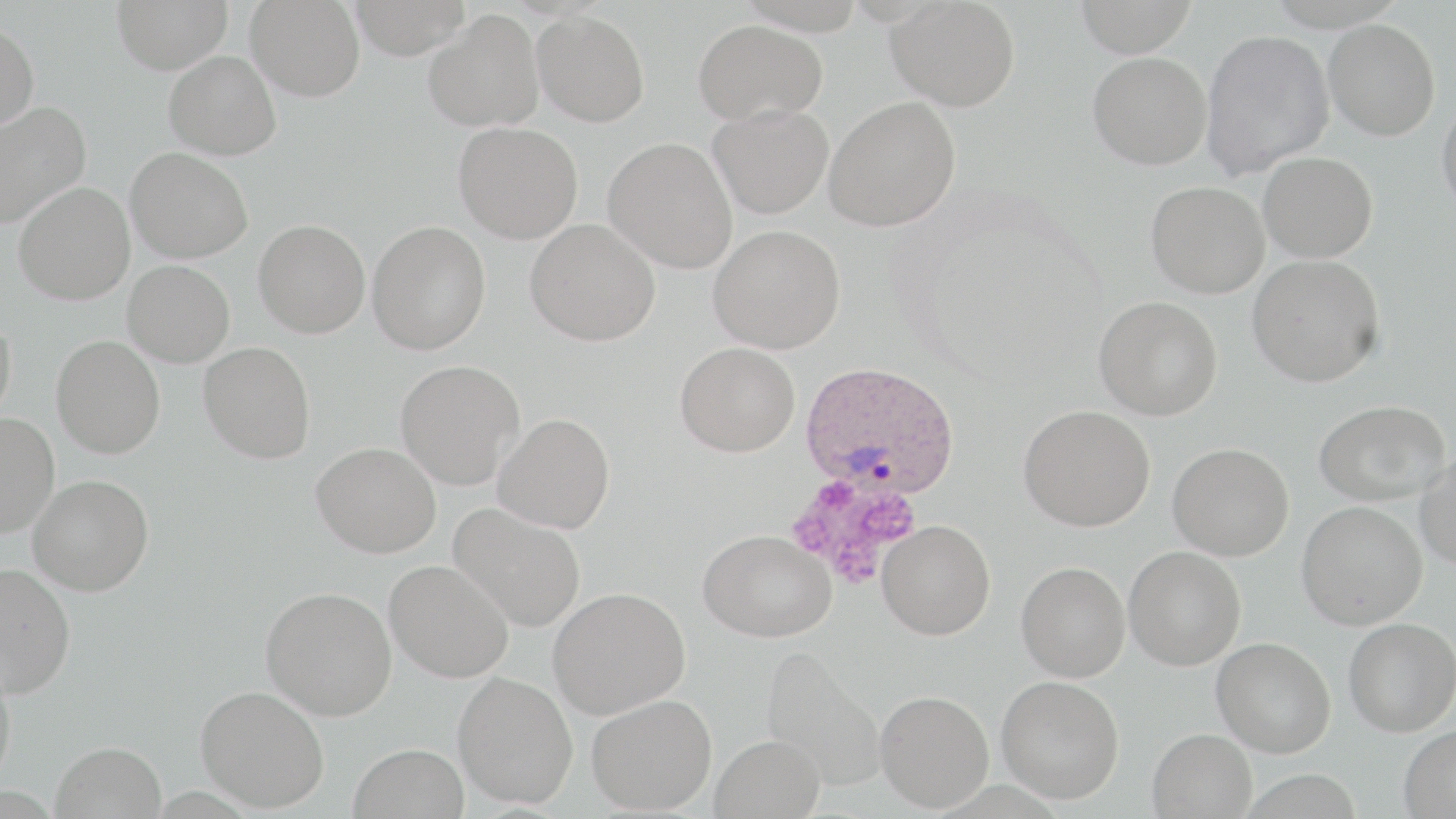
{
  "slide_level_diagnosis": "Plasmodium ovale",
  "preparation": "thin blood film",
  "modality": "optical microscopy",
  "stain": "May-Grünwald-Giemsa",
  "field_of_view": "single",
  "plasmodium_ovale_infected_red_blood_cell_locations": "approximate bounding boxes as (x1,y1)-(x2,y2) corner pairs in pixels: (801,360)-(960,495)",
  "image_size": "1456×819 pixels",
  "magnification": "1000x",
  "platelet_locations": "approximate bounding boxes as (x1,y1)-(x2,y2) corner pairs in pixels: (786,473)-(919,584)",
  "uninfected_red_blood_cell_locations": "approximate bounding boxes as (x1,y1)-(x2,y2) corner pairs in pixels: (112,0)-(232,74), (246,0)-(365,101), (346,0)-(472,60), (886,0)-(1020,112), (1072,0)-(1199,57), (423,10)-(545,132), (533,10)-(650,127), (1323,18)-(1440,140), (692,19)-(827,125), (0,21)-(39,134), (1201,29)-(1335,179), (164,51)-(281,160), (1088,52)-(1212,169), (1436,93)-(1456,222), (824,96)-(961,231), (0,101)-(91,230), (708,104)-(833,219), (454,122)-(583,244), (603,137)-(738,273), (125,147)-(253,263), (1258,152)-(1377,262), (13,181)-(135,305), (1146,181)-(1269,298), (254,219)-(370,338), (526,219)-(660,346), (367,220)-(491,355), (708,225)-(846,354), (1247,254)-(1385,387), (122,260)-(235,367), (1094,296)-(1222,420), (0,312)-(17,424), (51,335)-(166,458), (198,342)-(316,463), (675,342)-(800,456), (395,360)-(525,489), (1314,400)-(1450,505), (1018,404)-(1155,531), (0,412)-(59,538), (494,413)-(615,533), (312,442)-(441,557), (1168,443)-(1293,560), (1415,451)-(1456,570), (27,474)-(154,596), (1297,501)-(1427,629), (449,503)-(586,632), (877,520)-(996,640), (698,529)-(836,642), (1124,546)-(1246,670), (384,559)-(514,683), (1016,561)-(1130,681), (0,563)-(76,698), (261,585)-(396,720), (548,587)-(690,718), (1343,617)-(1456,736), (1211,636)-(1336,757), (760,644)-(887,791), (0,664)-(17,791), (453,671)-(578,809), (996,675)-(1125,804), (195,685)-(329,812), (875,690)-(994,811), (586,693)-(717,814), (1398,725)-(1456,819), (1147,728)-(1257,819), (710,735)-(825,819), (50,741)-(166,819), (348,742)-(469,819)"
}